State which parasite is depicted.
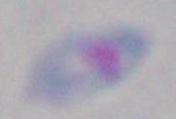
Toxoplasma gondii.

Captured at 1000x magnification. Photomicrograph.